Point out every Plasmodium parasite and every leukocyte.
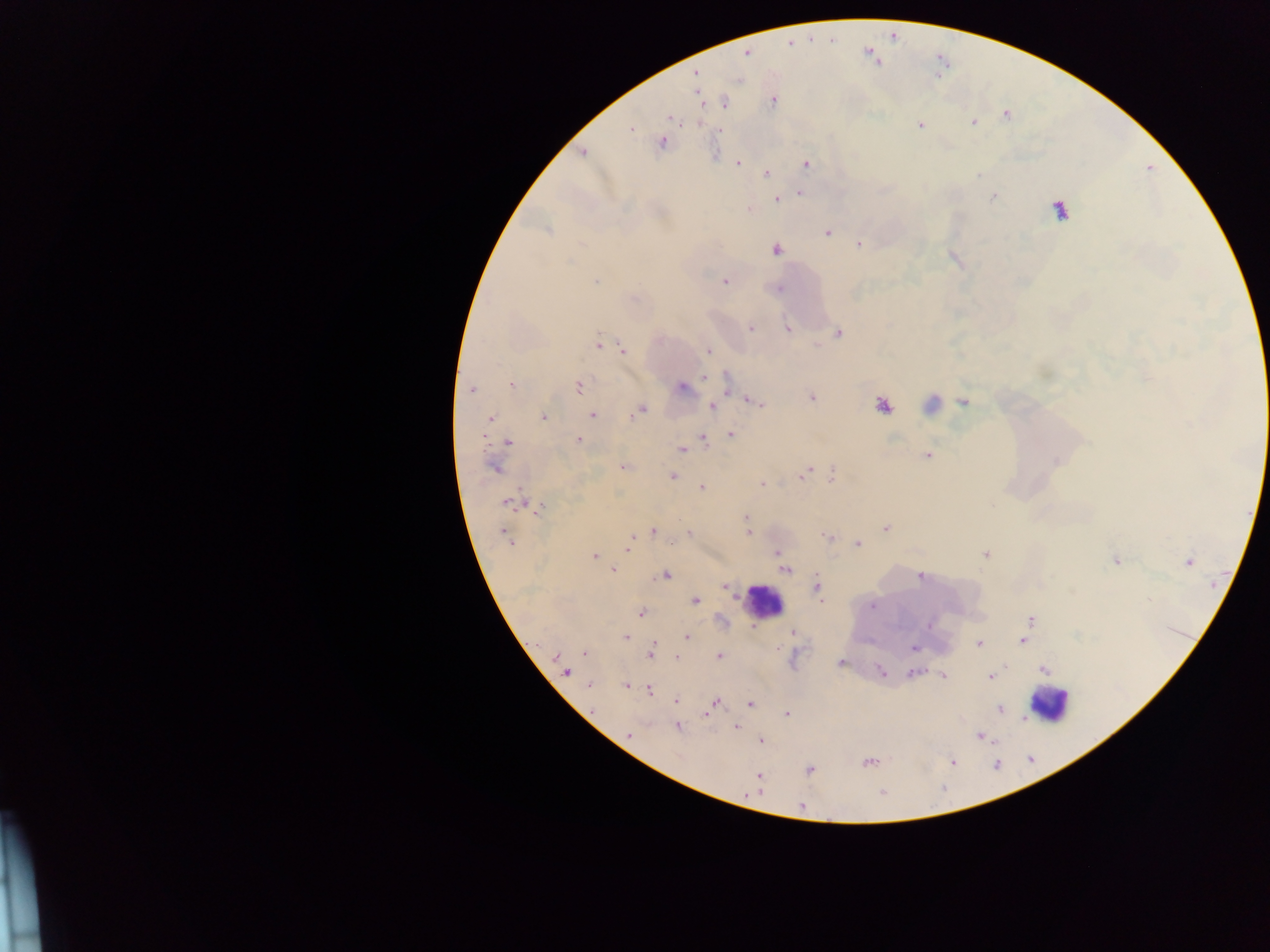
Approximate centers as (x, y) in pixels.
Plasmodium parasites: (746, 54), (695, 72), (699, 96), (773, 102), (724, 104), (1005, 115), (669, 117), (973, 123), (920, 125), (630, 128), (720, 132), (662, 142), (583, 151), (738, 163), (806, 163), (767, 173), (978, 175), (799, 193), (992, 197), (776, 200), (749, 209), (1058, 210), (547, 230), (827, 232), (858, 243), (775, 249), (725, 281), (595, 282), (779, 288), (751, 328), (787, 329), (839, 333), (599, 345), (623, 349), (708, 351), (705, 376), (512, 385), (578, 386), (682, 387), (472, 389), (812, 397), (750, 400), (964, 401), (758, 404), (882, 405), (712, 407), (640, 409), (593, 415), (544, 416), (489, 418), (730, 435), (483, 437), (703, 437), (579, 440), (508, 442), (682, 450), (927, 455), (493, 467), (621, 468), (803, 474), (832, 475), (671, 476), (800, 478), (762, 484), (701, 488), (508, 502), (539, 509), (746, 516), (886, 528), (653, 531), (689, 533), (748, 534), (505, 536), (826, 536), (630, 540), (509, 542), (858, 544), (628, 546), (776, 553), (985, 555), (594, 556), (1116, 560), (1189, 562), (614, 570), (786, 570), (665, 574), (920, 577), (725, 586), (816, 587), (695, 600), (873, 606), (641, 613), (1029, 621), (929, 625), (792, 633), (626, 637), (687, 637), (1023, 641), (978, 644), (652, 647), (913, 648), (584, 653), (650, 654), (556, 656), (720, 656), (676, 658), (840, 663), (880, 670), (1044, 670), (566, 671), (913, 673), (942, 676), (990, 676), (589, 684), (626, 686), (650, 691), (676, 701), (713, 704), (750, 704), (1000, 710), (707, 713), (787, 714), (678, 727), (736, 727), (629, 734), (979, 736), (760, 740), (868, 762), (953, 762), (810, 770), (759, 776), (801, 806).
Leukocytes: (932, 405), (764, 601), (1049, 705).

Summary:
  - Capture: mobile-phone photograph through a microscope
  - Country: Ghana
  - Field of view: single
  - Image size: 1270×952 pixels
  - Preparation: thick blood smear